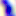

Summary:
  - Identification: Toxoplasma gondii
  - Modality: micrograph
  - Magnification: 400x